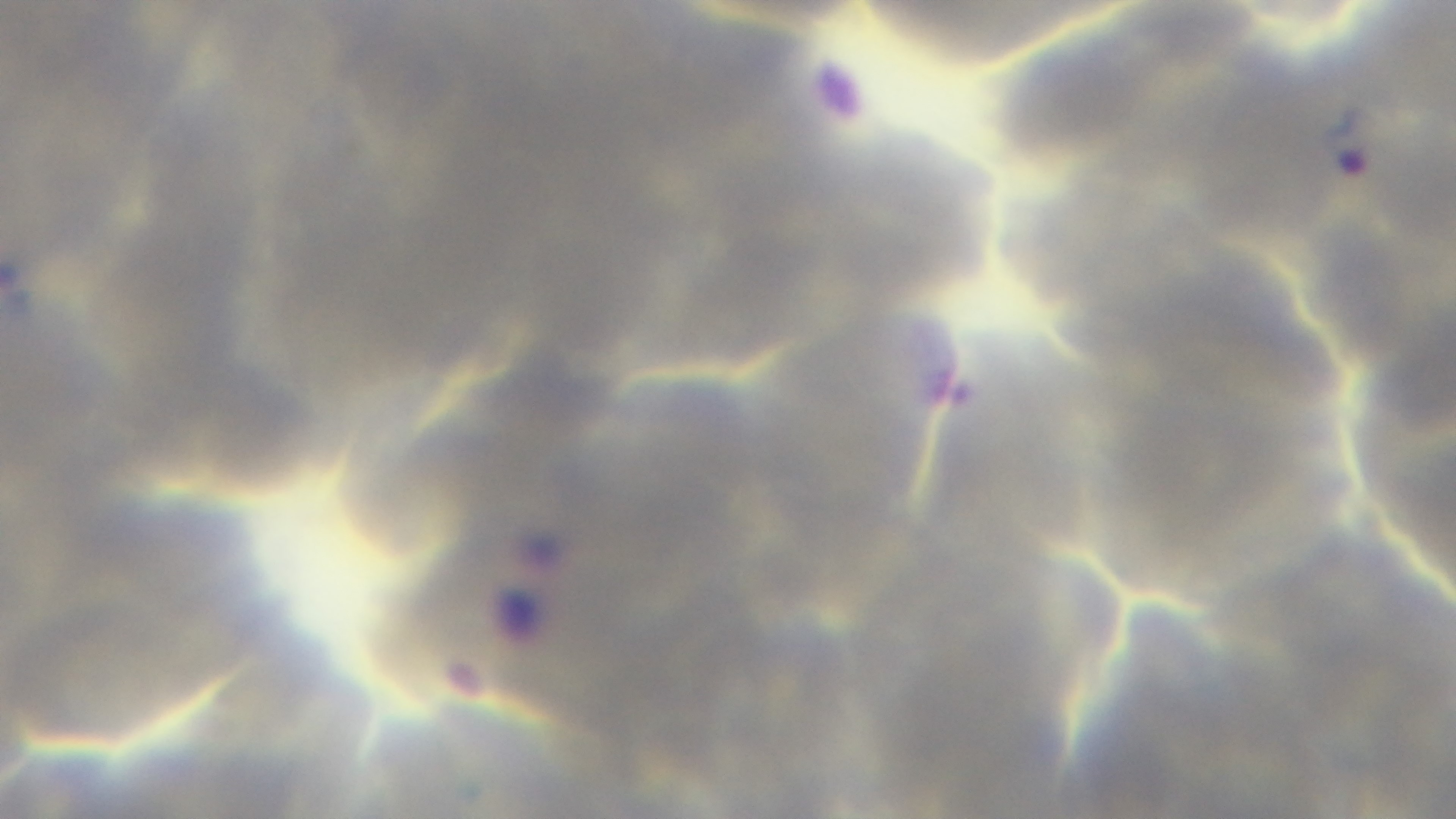

Photomicrograph. Oil-immersion objective, 100x. Preparation: thin. Single field of view. Malaria status: positive. Giemsa-stained. Mounted 4K digital camera.